Assess this cell for malaria.
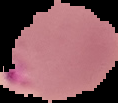

Parasitized.

Summary:
  - Image type: segmented cell region with the area outside set to black
  - Preparation: thin blood smear
  - Image size: 118×103 pixels